Describe the morphology of the erythrocytes.
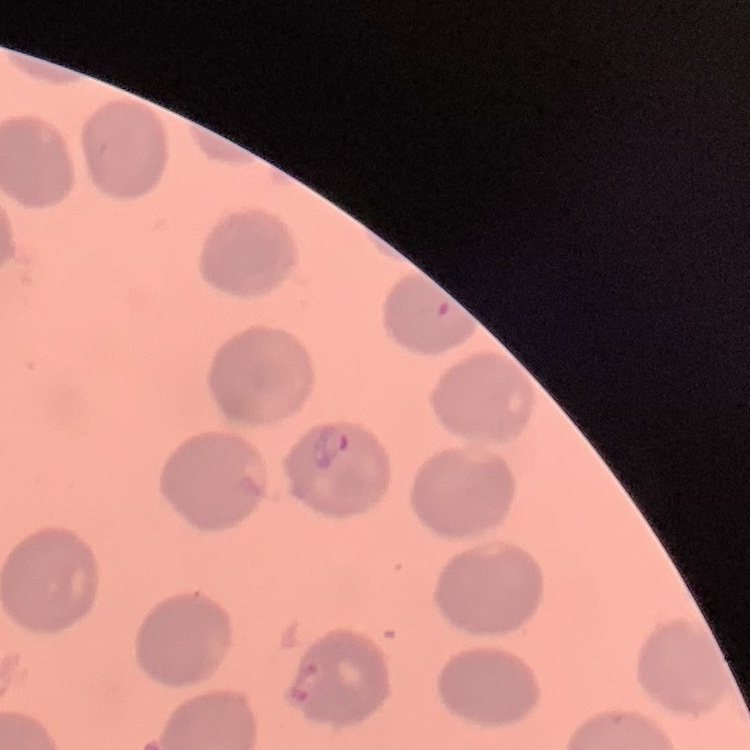

No rouleaux formation.

Summary:
  - Preparation: thin blood smear
  - Image type: square crop of a larger photomicrograph
  - Stain: Field's or Giemsa